Describe the morphology of the erythrocytes.
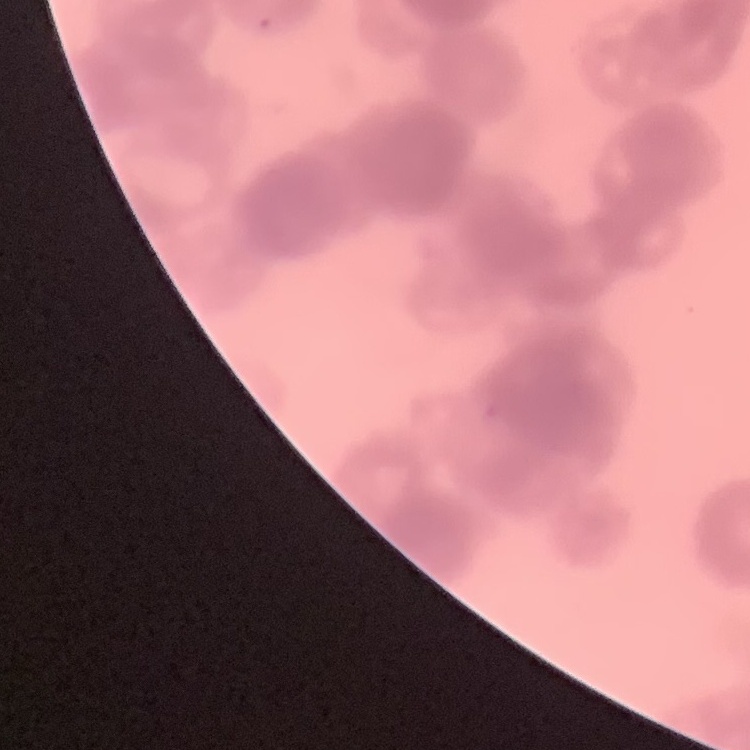
Rouleaux formation.

Summary:
  - Image type: one tile cut from a larger photomicrograph
  - Stain: Field's or Giemsa
  - Preparation: thin blood film